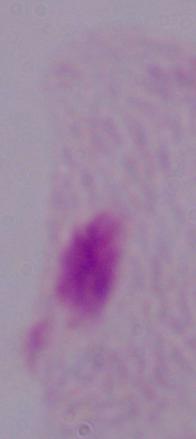 Micrograph. A trichomonad is shown. Captured at 1000x magnification.